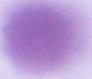

Summary:
  - Magnification: 1000x
  - Identification: erythrocyte
  - Modality: photomicrograph